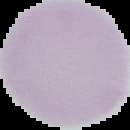
Summary:
  - Malaria status: uninfected
  - Preparation: thin blood smear
  - Image size: 130×130 pixels
  - Image type: cell region segmented out of the field of view; surrounding area masked to black